Classify this cell by malaria status.
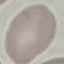

Uninfected.

Summary:
  - Stain: Giemsa
  - Capture: smartphone camera at the microscope eyepiece
  - Preparation: thin smear
  - Image type: automatically extracted cell patch, resized to 64 × 64 pixels